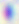 400x magnification. Toxoplasma gondii is shown. Photomicrograph.